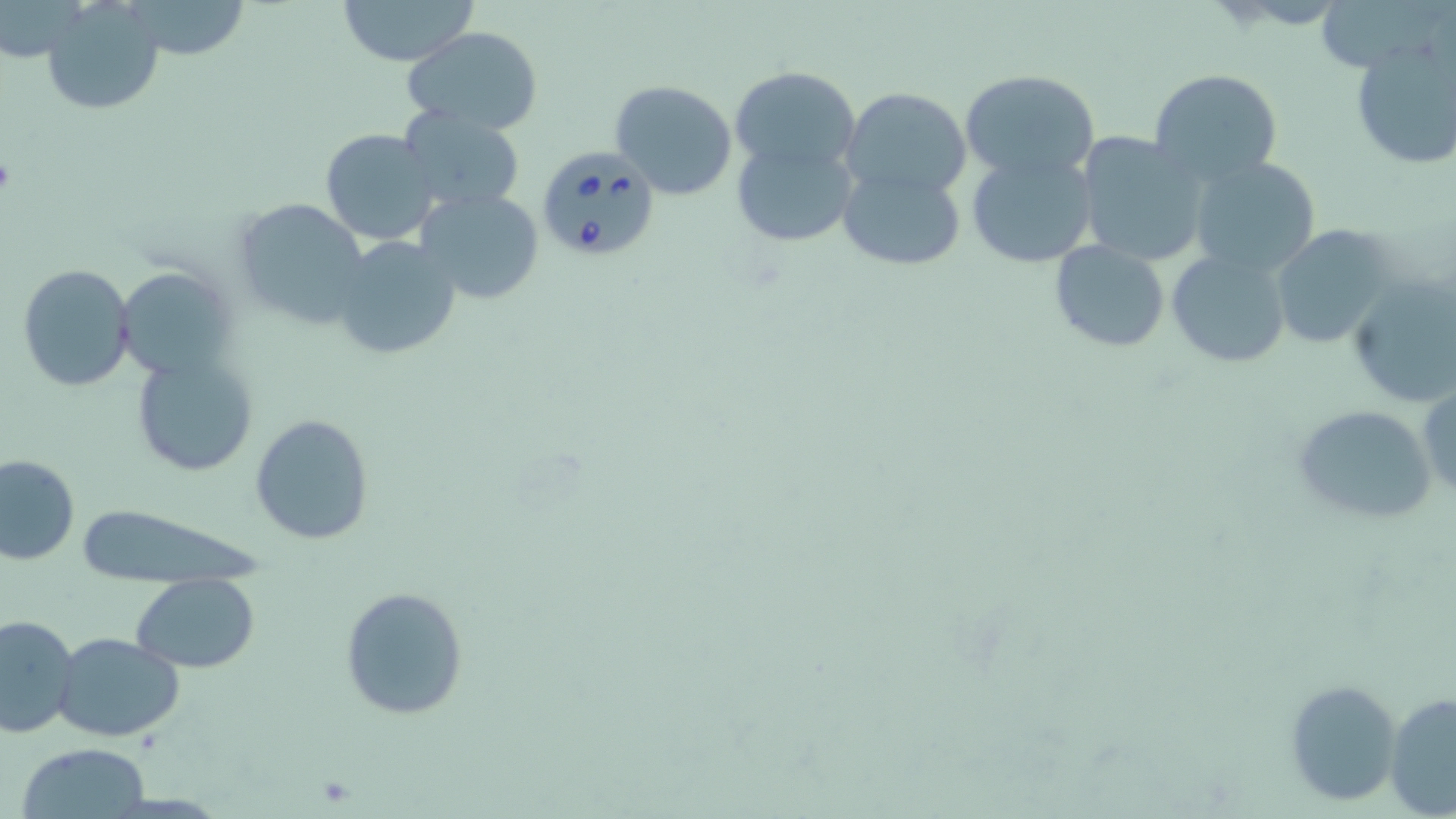

Summary:
  - Coordinate format: approximate bounding boxes as [x1, y1, x2, y2] in pixels
  - Babesia divergens-infected red blood cell locations: [535, 144, 662, 262]
  - Uninfected red blood cell locations: [132, 0, 248, 61], [338, 0, 479, 68], [42, 1, 164, 116], [403, 27, 546, 134], [1348, 39, 1456, 171], [729, 66, 860, 179], [959, 67, 1100, 186], [1148, 68, 1284, 190], [611, 81, 739, 201], [841, 86, 971, 199], [398, 106, 526, 213], [319, 128, 441, 245], [1074, 131, 1211, 269], [731, 137, 858, 247], [965, 149, 1098, 268], [1189, 155, 1323, 278], [836, 164, 967, 270], [413, 187, 546, 307], [231, 198, 372, 331], [1271, 224, 1399, 349], [330, 233, 464, 361], [1049, 239, 1172, 352], [1166, 247, 1291, 368], [19, 265, 135, 392], [113, 267, 234, 381], [1347, 279, 1456, 410], [133, 356, 258, 478], [1418, 380, 1456, 506], [1292, 402, 1437, 526], [250, 414, 375, 544], [0, 454, 79, 564], [72, 504, 263, 591], [131, 574, 260, 672], [339, 586, 470, 722], [0, 614, 81, 740], [54, 632, 186, 744], [1283, 678, 1403, 806], [1386, 690, 1456, 818], [16, 742, 150, 817]
  - Slide-level diagnosis: Babesia divergens
  - Stain: May-Grünwald-Giemsa
  - Magnification: 1000x
  - Modality: optical microscopy
  - Image size: 1456×819 pixels
  - Preparation: thin blood smear
  - Field of view: single